Outline each blood parasite and name the species.
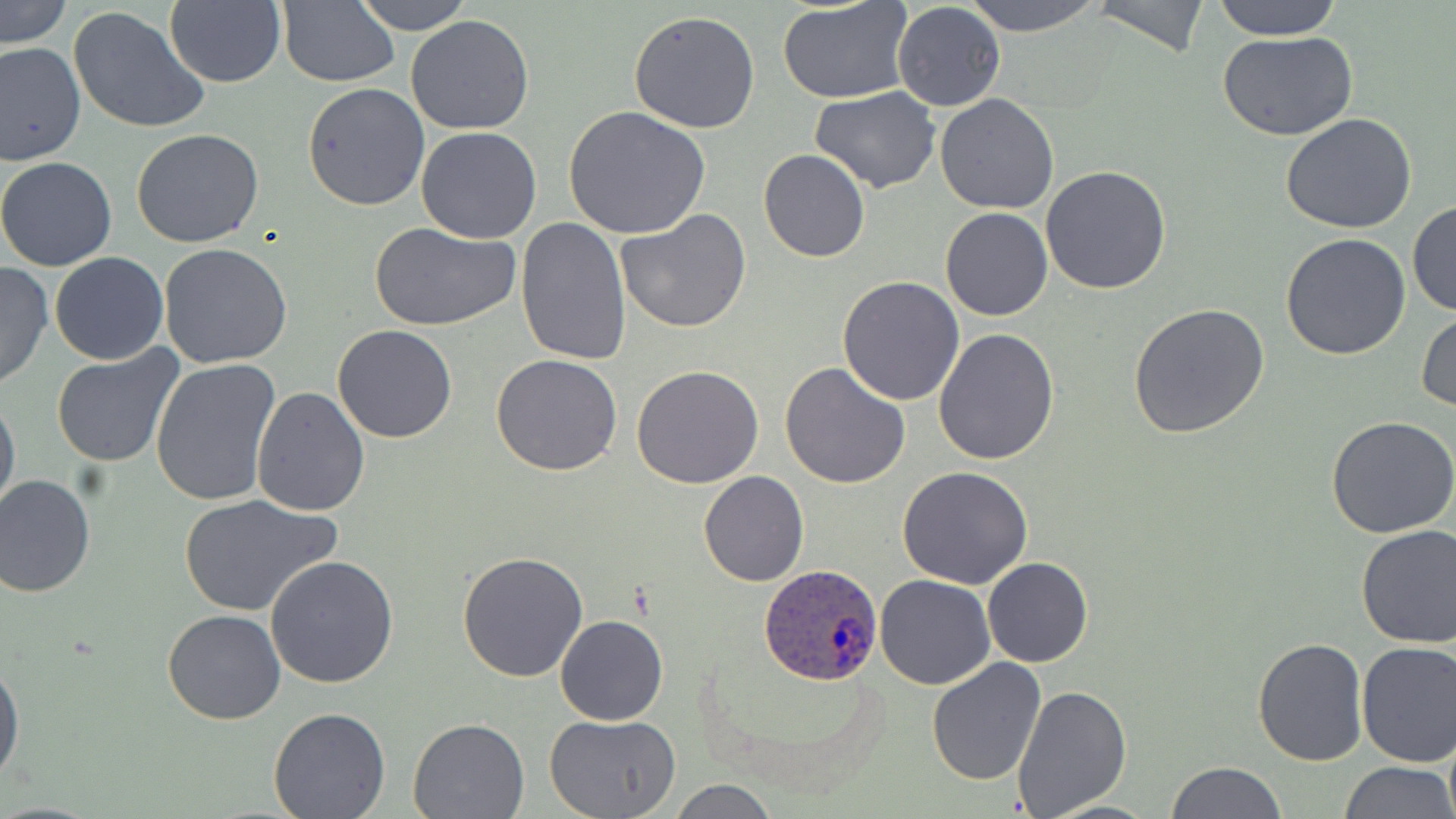

Approximate bounding boxes as (x1,y1)-(x2,y2) corner pairs in pixels.
Plasmodium ovale-infected red blood cells: (760,563)-(883,684).
No Plasmodium falciparum, Plasmodium malariae, Plasmodium vivax, Babesia divergens, or Trypanosoma brucei observed.

{
  "slide_level_diagnosis": "Plasmodium ovale",
  "preparation": "thin blood smear",
  "magnification": "1000x",
  "uninfected_red_blood_cell_locations": "approximate bounding boxes as (x1,y1)-(x2,y2) corner pairs in pixels: (2,0)-(71,50), (351,0)-(472,35), (964,0)-(1102,37), (1090,0)-(1211,60), (1210,0)-(1345,40), (164,1)-(285,87), (278,1)-(400,87), (777,2)-(915,104), (892,3)-(1005,113), (67,5)-(212,135), (629,10)-(761,134), (404,15)-(534,135), (1217,30)-(1358,142), (1,41)-(85,166), (302,82)-(431,212), (811,87)-(942,194), (934,94)-(1059,214), (563,106)-(712,240), (1279,112)-(1417,234), (416,127)-(543,245), (131,128)-(264,248), (758,149)-(870,262), (0,156)-(117,272), (1040,166)-(1172,295), (1407,198)-(1456,316), (940,206)-(1052,321), (617,209)-(752,333), (516,216)-(631,366), (367,219)-(520,332), (1279,233)-(1411,360), (159,244)-(293,369), (49,253)-(169,365), (0,262)-(52,392), (838,276)-(965,406), (1128,303)-(1269,439), (1416,309)-(1456,416), (333,325)-(456,443), (934,329)-(1059,465), (51,346)-(186,467), (491,355)-(623,477), (150,359)-(281,508), (781,362)-(910,487), (632,365)-(763,487), (251,385)-(372,517), (0,393)-(20,519), (1327,415)-(1456,538), (898,465)-(1033,588), (699,470)-(808,586), (0,472)-(96,598), (177,492)-(341,617), (1355,523)-(1456,647), (457,551)-(589,684), (265,555)-(400,689), (983,557)-(1093,668), (876,575)-(995,690), (163,610)-(286,725), (556,615)-(668,726), (1253,638)-(1368,766), (1355,641)-(1456,768), (927,658)-(1047,786), (0,659)-(23,784), (1012,685)-(1132,817), (267,708)-(391,819), (544,714)-(680,819), (408,716)-(531,818), (1166,761)-(1286,818), (1340,761)-(1453,818), (669,779)-(778,818)",
  "stain": "May-Grünwald-Giemsa",
  "field_of_view": "single",
  "image_size": "1456×819 pixels",
  "modality": "light microscopy"
}